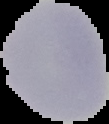
result: negative for malaria parasites
image_type: segmented cell region on a black background
image_size: 109×124 pixels
preparation: thin blood film